Identify the parasite.
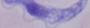
A trypanosome.

magnification = 1000x
modality = micrograph